Report the malaria status of this cell.
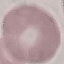

It is uninfected.

Summary:
  - Preparation: thin blood smear
  - Stain: Giemsa
  - Capture: smartphone camera at the microscope eyepiece
  - Image type: cell patch, automatically extracted from a larger field of view and resized to 64 × 64 pixels